Locate every malaria parasite.
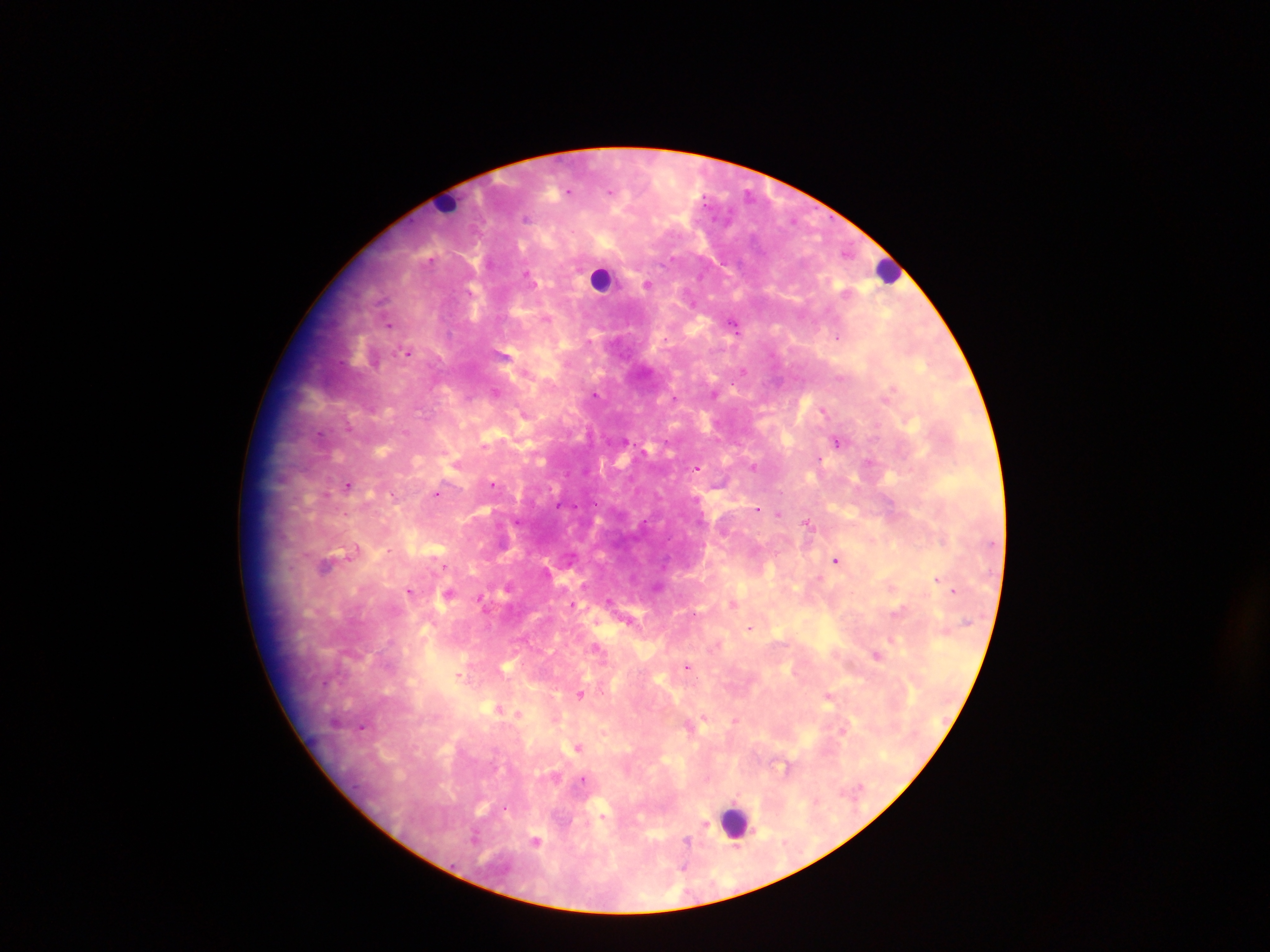
Approximate centers as [x, y] in pixels.
Malaria parasites: [571, 189], [526, 218], [429, 256], [527, 273], [647, 284], [381, 298], [548, 320], [734, 324], [392, 326], [837, 336], [408, 352], [504, 353], [743, 371], [892, 387], [714, 390], [496, 392], [596, 393], [824, 408], [521, 412], [522, 417], [320, 435], [623, 440], [837, 441], [454, 462], [869, 462], [753, 465], [696, 467], [494, 484], [349, 486], [437, 494], [757, 510], [780, 512], [806, 523], [353, 551], [836, 559], [328, 562], [445, 566], [819, 578], [938, 578], [509, 585], [658, 586], [893, 588], [411, 591], [954, 591], [610, 601], [735, 602], [574, 606], [900, 610], [751, 627], [893, 639], [597, 648], [878, 657], [508, 664], [688, 666], [459, 675], [580, 692], [828, 694], [493, 711], [501, 713], [519, 715], [706, 717], [735, 719], [364, 724], [844, 731], [577, 747], [785, 767], [581, 780], [706, 824], [535, 838], [688, 839].

Leukocyte locations: [447, 202], [889, 271], [602, 281], [735, 819]. Single field of view. Mobile-phone photograph taken through the microscope. Image is 1270×952 pixels. Sample from Ghana. Thick blood film.